Point out each Plasmodium parasite.
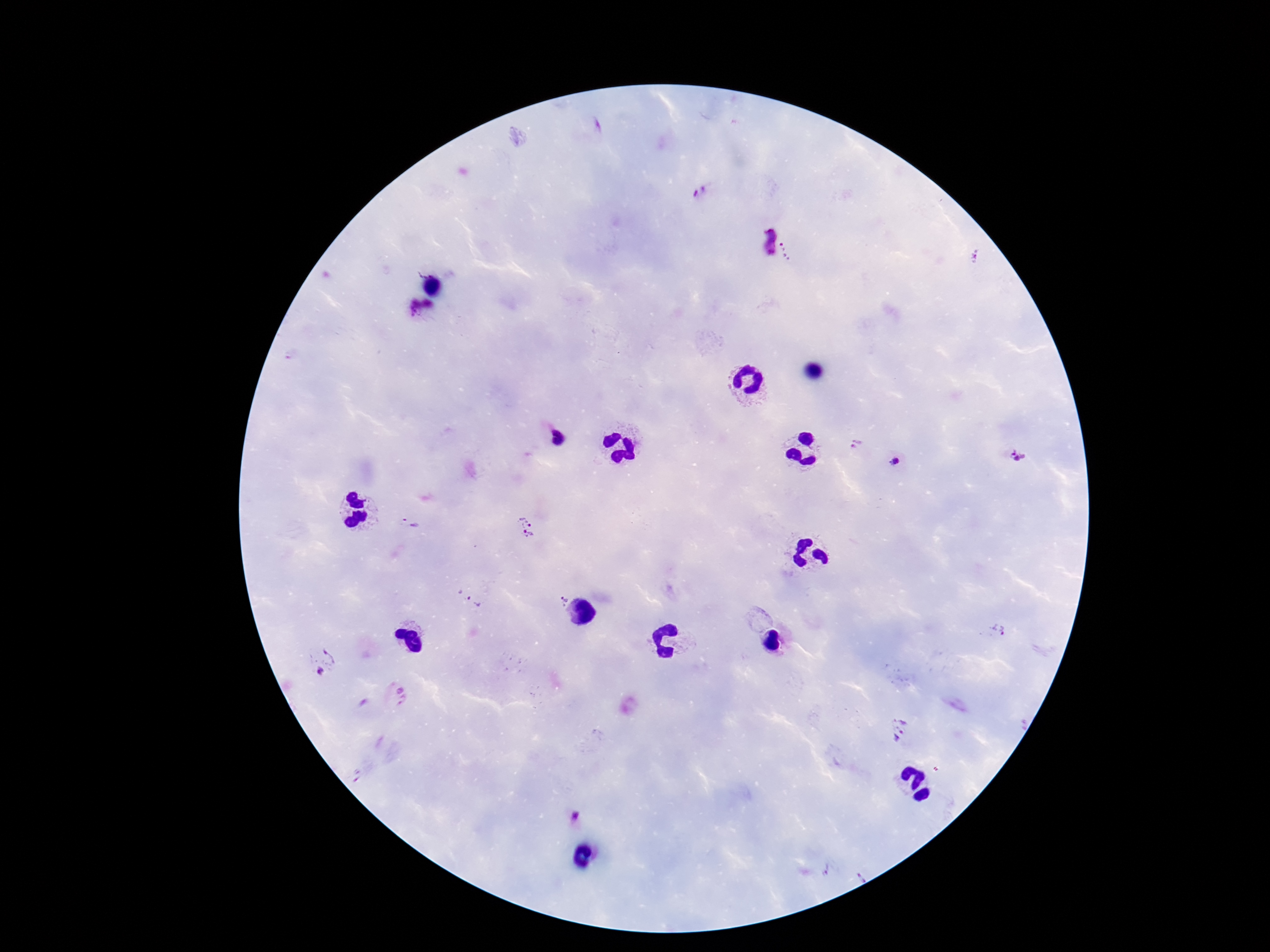

Approximate centers as (x, y) in pixels.
Plasmodium parasites: (701, 190), (769, 242), (791, 250), (976, 256), (421, 311), (856, 444), (1017, 456), (895, 462), (409, 523), (525, 527), (561, 596), (468, 597), (996, 629), (323, 660), (398, 695), (901, 729), (575, 814).

capture = smartphone camera through the microscope eyepiece
image size = 1270×952 pixels
preparation = thick blood smear
field of view = one from this slide
stain = Giemsa
magnification = 100x
patient malaria status = infected